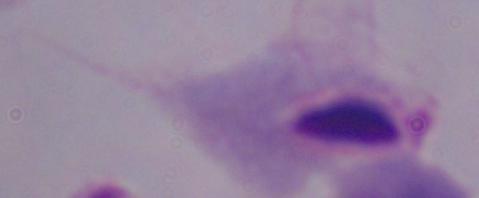
magnification = 1000x
modality = micrograph
identification = trichomonad